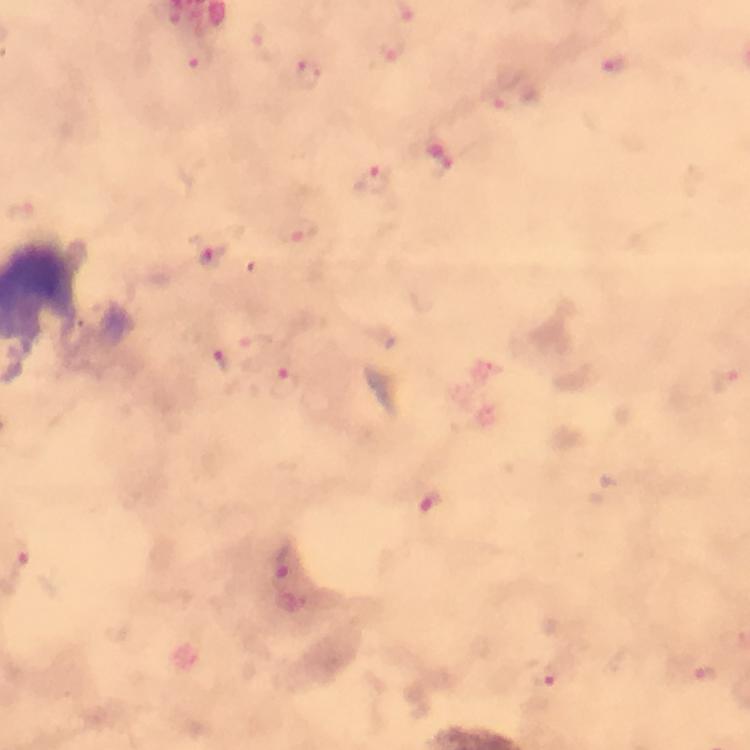 Approximate centers as [x, y] in pixels. Plasmodium parasite locations: [263, 39], [393, 46], [197, 58], [616, 64], [307, 73], [500, 100], [445, 170], [374, 178], [19, 212], [297, 231], [208, 249], [250, 348], [282, 368], [725, 381], [431, 503], [20, 556], [286, 559], [707, 673], [545, 677]. At 100x magnification. Giemsa-stained preparation. Thick blood film. Immersion oil was used. Photographed through the microscope with a smartphone camera. A crop from one field of view. Image is 750×750 pixels. From a malaria diagnostic workup.